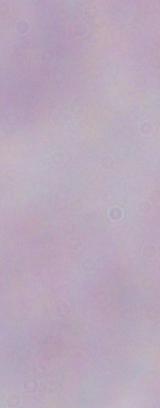 A trypanosome is seen. Photomicrograph. 1000x magnification.